Locate every uninfected red blood cell.
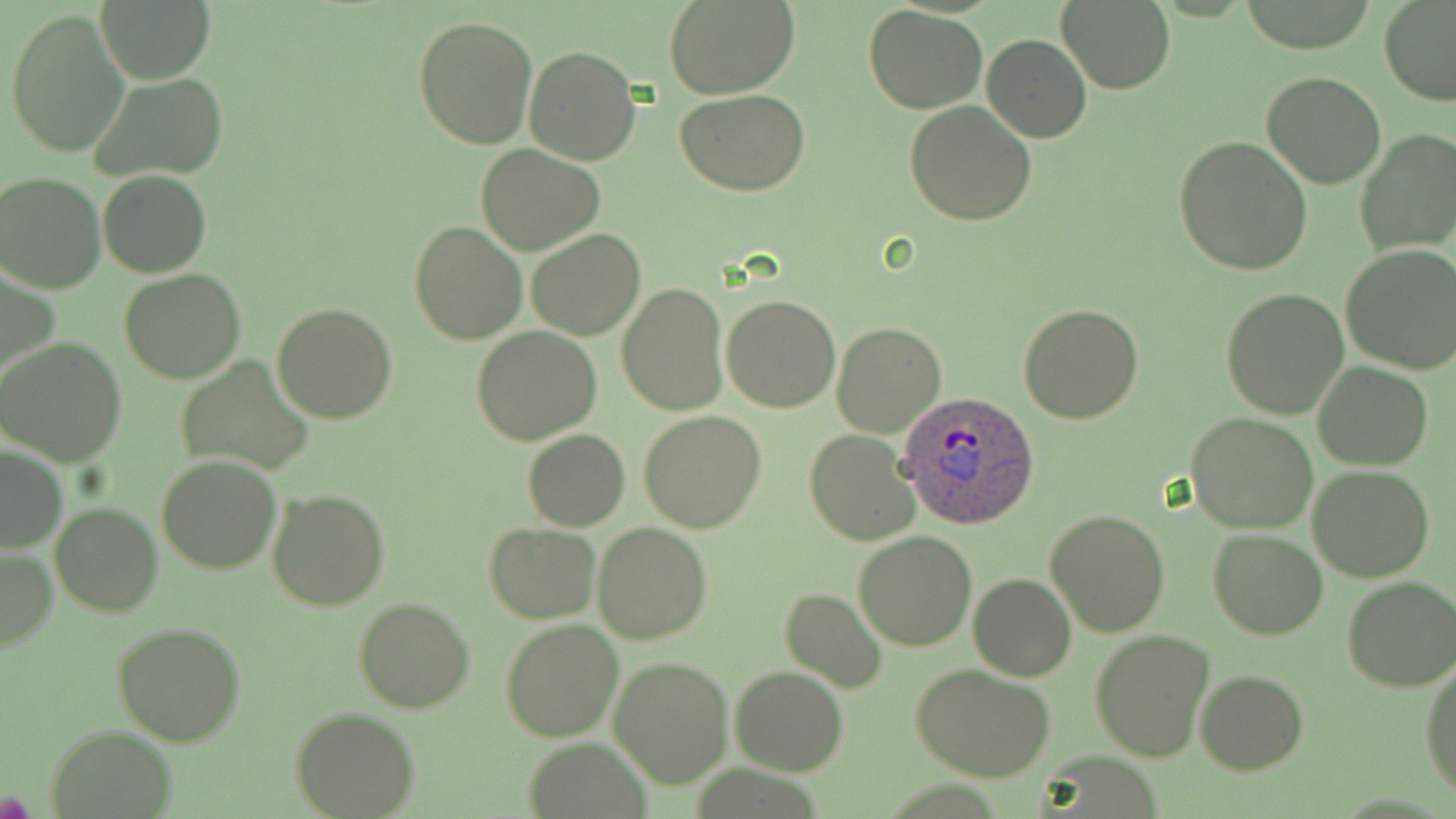

Approximate bounding boxes as named x1/y1/x2/y2 corners in pixels.
Uninfected red blood cells: (x1=664, y1=0, x2=800, y2=99), (x1=97, y1=1, x2=214, y2=84), (x1=1057, y1=1, x2=1175, y2=93), (x1=1378, y1=2, x2=1456, y2=107), (x1=864, y1=5, x2=987, y2=113), (x1=5, y1=7, x2=131, y2=158), (x1=413, y1=15, x2=538, y2=150), (x1=981, y1=34, x2=1093, y2=142), (x1=523, y1=44, x2=639, y2=165), (x1=1262, y1=70, x2=1385, y2=189), (x1=90, y1=73, x2=230, y2=185), (x1=676, y1=88, x2=809, y2=196), (x1=905, y1=101, x2=1036, y2=225), (x1=1355, y1=128, x2=1456, y2=256), (x1=1173, y1=136, x2=1313, y2=274), (x1=475, y1=145, x2=604, y2=256), (x1=0, y1=170, x2=106, y2=293), (x1=97, y1=170, x2=212, y2=277), (x1=408, y1=220, x2=527, y2=346), (x1=527, y1=229, x2=646, y2=340), (x1=1337, y1=244, x2=1456, y2=376), (x1=2, y1=263, x2=57, y2=388), (x1=119, y1=269, x2=246, y2=383), (x1=617, y1=283, x2=728, y2=415), (x1=1222, y1=286, x2=1350, y2=419), (x1=721, y1=294, x2=841, y2=413), (x1=1018, y1=302, x2=1145, y2=425), (x1=272, y1=303, x2=397, y2=424), (x1=831, y1=321, x2=946, y2=437), (x1=471, y1=324, x2=602, y2=446), (x1=0, y1=337, x2=128, y2=466), (x1=174, y1=355, x2=315, y2=476), (x1=1314, y1=362, x2=1434, y2=470), (x1=639, y1=411, x2=766, y2=532), (x1=1187, y1=413, x2=1317, y2=534), (x1=523, y1=428, x2=630, y2=532), (x1=805, y1=431, x2=920, y2=546), (x1=0, y1=445, x2=67, y2=555), (x1=155, y1=455, x2=283, y2=574), (x1=1309, y1=465, x2=1435, y2=583), (x1=265, y1=487, x2=391, y2=611), (x1=49, y1=502, x2=162, y2=617), (x1=1046, y1=509, x2=1170, y2=637), (x1=591, y1=521, x2=711, y2=643), (x1=484, y1=523, x2=600, y2=624), (x1=1207, y1=528, x2=1328, y2=639), (x1=853, y1=530, x2=977, y2=652), (x1=0, y1=546, x2=57, y2=652), (x1=969, y1=572, x2=1076, y2=681), (x1=1341, y1=577, x2=1456, y2=694), (x1=781, y1=587, x2=888, y2=693), (x1=354, y1=597, x2=474, y2=713), (x1=500, y1=618, x2=624, y2=742), (x1=111, y1=622, x2=246, y2=747), (x1=1089, y1=629, x2=1216, y2=762), (x1=1421, y1=654, x2=1456, y2=799), (x1=611, y1=656, x2=733, y2=786), (x1=910, y1=664, x2=1056, y2=782), (x1=731, y1=666, x2=847, y2=776), (x1=1195, y1=670, x2=1309, y2=774), (x1=290, y1=705, x2=421, y2=818), (x1=48, y1=728, x2=176, y2=816), (x1=520, y1=738, x2=654, y2=819).

Plasmodium ovale-infected red blood cell locations: (x1=897, y1=390, x2=1038, y2=529). Slide-level diagnosis: Plasmodium ovale. Single field of view. Optical microscopy. May-Grünwald-Giemsa stain. Image is 1456×819 pixels. Thin blood film. 1000x magnification.